Classify this cell by malaria status.
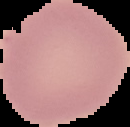
It is uninfected.

Summary:
  - Image size: 130×127 pixels
  - Preparation: thin blood film
  - Image type: segmented cell region on a black background